State which parasite is depicted.
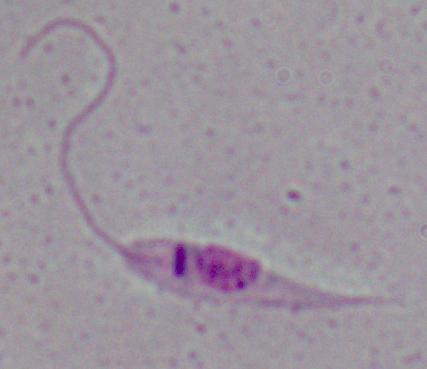

This is Leishmania.

Summary:
  - Modality: micrograph
  - Magnification: 1000x